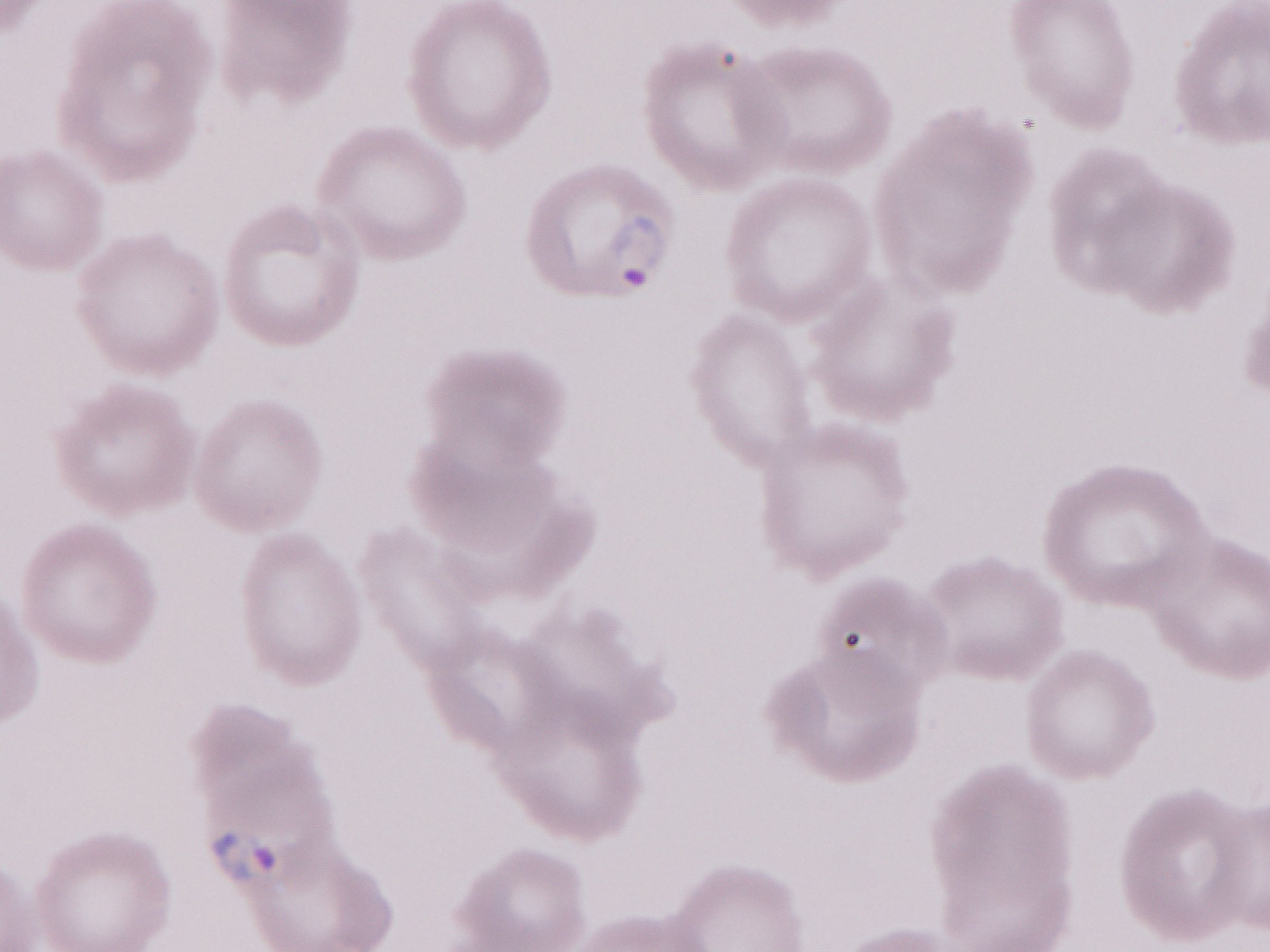
Olympus BX43 microscope, Olympus DP73 camera. May-Grünwald-Giemsa (MGG) stain. Thin blood smear. Magnification: 1,000x. Image is 1270×952 pixels. One field of this slide. Malaria diagnosis (patient-level): positive.